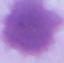
identification = erythrocyte
magnification = 1000x
modality = micrograph